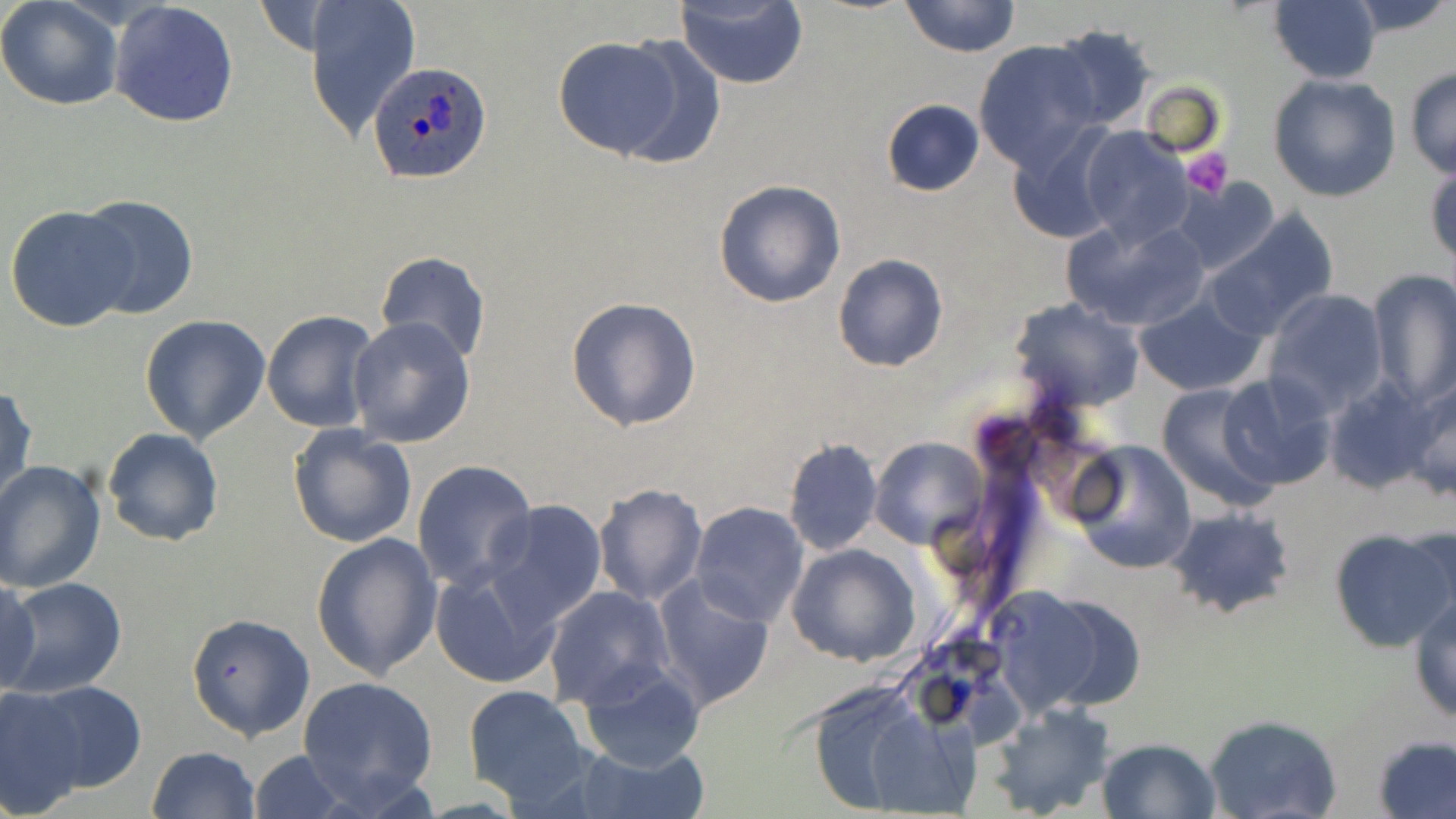
Summary:
  - Coordinate format: approximate bounding boxes as named x1/y1/x2/y2 corners in pixels
  - Plasmodium ovale-infected red blood cell locations: (x1=368, y1=63, x2=492, y2=186)
  - Uninfected red blood cell locations: (x1=0, y1=0, x2=125, y2=113), (x1=304, y1=0, x2=421, y2=142), (x1=899, y1=0, x2=1019, y2=58), (x1=1339, y1=0, x2=1453, y2=36), (x1=675, y1=1, x2=809, y2=89), (x1=1266, y1=1, x2=1382, y2=84), (x1=109, y1=2, x2=240, y2=127), (x1=1049, y1=26, x2=1157, y2=131), (x1=553, y1=36, x2=691, y2=159), (x1=973, y1=40, x2=1103, y2=173), (x1=1403, y1=67, x2=1456, y2=179), (x1=1267, y1=75, x2=1402, y2=204), (x1=1139, y1=81, x2=1225, y2=156), (x1=880, y1=99, x2=985, y2=197), (x1=1007, y1=124, x2=1123, y2=243), (x1=1078, y1=127, x2=1193, y2=247), (x1=1426, y1=164, x2=1456, y2=270), (x1=1175, y1=178, x2=1281, y2=275), (x1=713, y1=179, x2=845, y2=307), (x1=75, y1=194, x2=199, y2=320), (x1=6, y1=204, x2=137, y2=334), (x1=1203, y1=210, x2=1339, y2=340), (x1=1062, y1=215, x2=1211, y2=333), (x1=374, y1=251, x2=490, y2=367), (x1=832, y1=253, x2=950, y2=371), (x1=1365, y1=269, x2=1456, y2=411), (x1=1263, y1=289, x2=1389, y2=416), (x1=1133, y1=294, x2=1268, y2=397), (x1=566, y1=297, x2=702, y2=431), (x1=1009, y1=298, x2=1145, y2=412), (x1=262, y1=309, x2=378, y2=433), (x1=139, y1=315, x2=272, y2=444), (x1=347, y1=317, x2=476, y2=447), (x1=1218, y1=371, x2=1337, y2=491), (x1=1400, y1=374, x2=1456, y2=502), (x1=1323, y1=376, x2=1436, y2=493), (x1=1156, y1=381, x2=1284, y2=513), (x1=0, y1=383, x2=37, y2=508), (x1=287, y1=423, x2=418, y2=550), (x1=103, y1=427, x2=224, y2=546), (x1=783, y1=437, x2=884, y2=556), (x1=870, y1=437, x2=987, y2=550), (x1=1066, y1=439, x2=1198, y2=575), (x1=0, y1=459, x2=106, y2=594), (x1=412, y1=459, x2=540, y2=594), (x1=592, y1=483, x2=706, y2=605), (x1=483, y1=501, x2=607, y2=628), (x1=689, y1=502, x2=811, y2=627), (x1=1164, y1=505, x2=1296, y2=619), (x1=1405, y1=520, x2=1453, y2=633), (x1=1328, y1=526, x2=1456, y2=652), (x1=311, y1=531, x2=442, y2=681), (x1=787, y1=543, x2=921, y2=666), (x1=429, y1=566, x2=561, y2=690), (x1=0, y1=576, x2=42, y2=698), (x1=4, y1=577, x2=127, y2=698), (x1=654, y1=578, x2=775, y2=711), (x1=985, y1=582, x2=1146, y2=722), (x1=543, y1=586, x2=676, y2=711), (x1=1408, y1=594, x2=1456, y2=724), (x1=184, y1=612, x2=315, y2=740), (x1=576, y1=662, x2=705, y2=773), (x1=299, y1=675, x2=439, y2=808), (x1=27, y1=679, x2=148, y2=792), (x1=463, y1=684, x2=593, y2=808), (x1=800, y1=685, x2=956, y2=818), (x1=1, y1=687, x2=87, y2=817), (x1=985, y1=700, x2=1114, y2=819), (x1=1202, y1=714, x2=1345, y2=819), (x1=1372, y1=735, x2=1456, y2=819), (x1=1096, y1=738, x2=1221, y2=819), (x1=567, y1=742, x2=706, y2=819), (x1=146, y1=745, x2=260, y2=819), (x1=249, y1=749, x2=350, y2=819)
  - Platelet locations: (x1=1180, y1=147, x2=1233, y2=198)
  - Slide-level diagnosis: Plasmodium ovale
  - Modality: light microscopy
  - Image size: 1456×819 pixels
  - Stain: May-Grünwald-Giemsa
  - Magnification: 1000x
  - Field of view: one of a larger specimen
  - Preparation: thin blood film